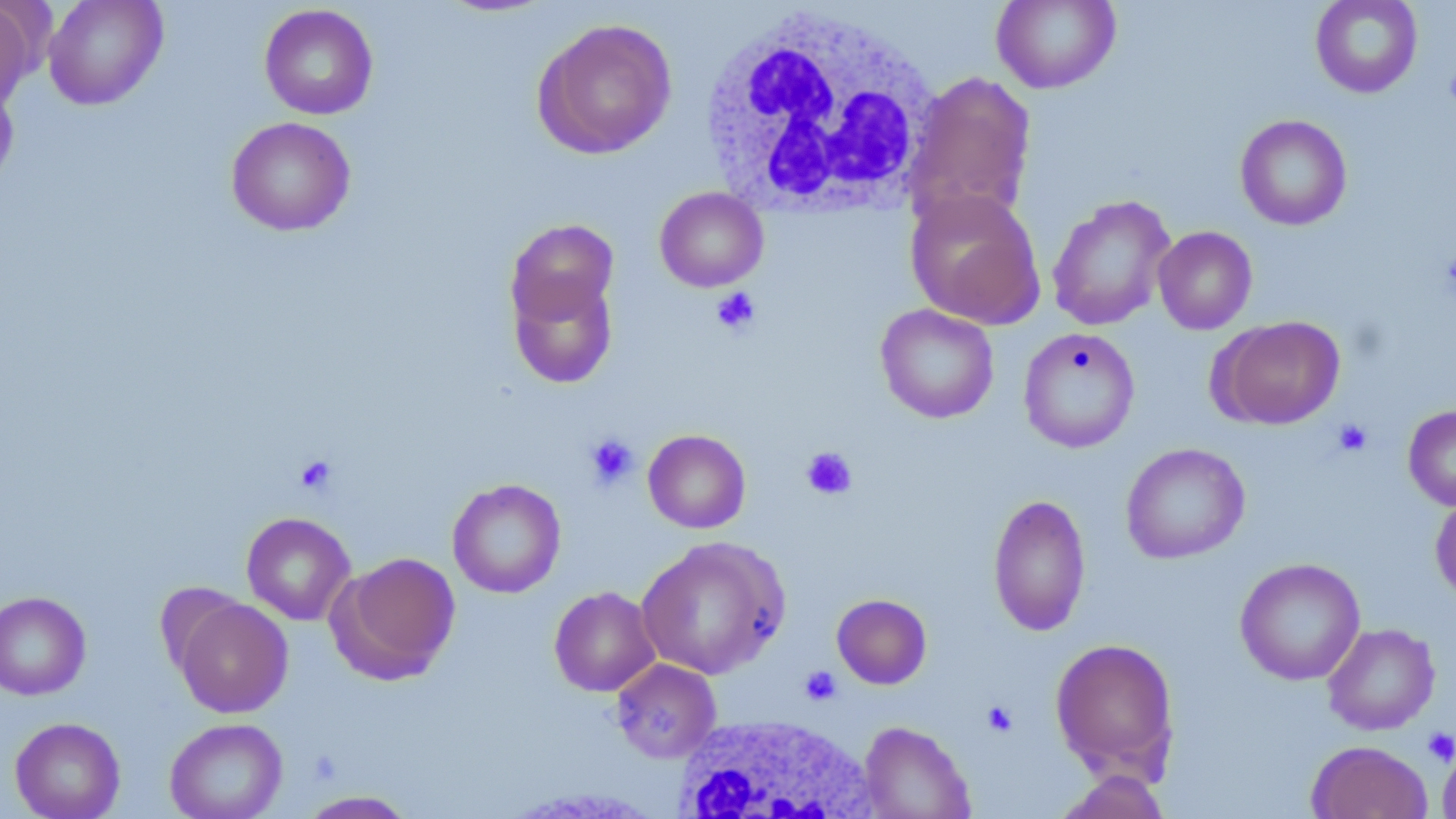

{
  "slide_level_diagnosis": "no evidence of blood parasites",
  "modality": "optical microscopy",
  "preparation": "thin blood smear",
  "uninfected_red_blood_cell_locations": "approximate bounding boxes as named x1/y1/x2/y2 corners in pixels: (x1=42, y1=0, x2=168, y2=110), (x1=991, y1=0, x2=1120, y2=93), (x1=1310, y1=0, x2=1423, y2=98), (x1=0, y1=1, x2=37, y2=114), (x1=259, y1=4, x2=379, y2=120), (x1=533, y1=17, x2=677, y2=160), (x1=904, y1=71, x2=1038, y2=229), (x1=0, y1=76, x2=20, y2=193), (x1=1235, y1=114, x2=1352, y2=231), (x1=225, y1=116, x2=356, y2=236), (x1=655, y1=186, x2=768, y2=292), (x1=906, y1=188, x2=1046, y2=330), (x1=1047, y1=194, x2=1176, y2=331), (x1=505, y1=219, x2=620, y2=330), (x1=1153, y1=226, x2=1257, y2=334), (x1=506, y1=265, x2=619, y2=389), (x1=875, y1=304, x2=999, y2=424), (x1=1214, y1=315, x2=1345, y2=429), (x1=1018, y1=327, x2=1140, y2=453), (x1=1403, y1=405, x2=1456, y2=511), (x1=643, y1=429, x2=751, y2=533), (x1=1120, y1=442, x2=1250, y2=564), (x1=447, y1=479, x2=566, y2=599), (x1=1430, y1=492, x2=1456, y2=605), (x1=987, y1=493, x2=1092, y2=637), (x1=241, y1=512, x2=356, y2=625), (x1=635, y1=537, x2=789, y2=680), (x1=331, y1=551, x2=461, y2=683), (x1=1235, y1=557, x2=1365, y2=685), (x1=549, y1=586, x2=661, y2=697), (x1=0, y1=591, x2=91, y2=701), (x1=832, y1=593, x2=932, y2=689), (x1=173, y1=597, x2=293, y2=718), (x1=1322, y1=622, x2=1440, y2=735), (x1=1049, y1=638, x2=1181, y2=784), (x1=611, y1=658, x2=722, y2=763), (x1=10, y1=717, x2=126, y2=819), (x1=164, y1=717, x2=288, y2=819), (x1=859, y1=721, x2=975, y2=819), (x1=1306, y1=740, x2=1433, y2=819), (x1=1436, y1=740, x2=1456, y2=818), (x1=1052, y1=769, x2=1173, y2=819), (x1=296, y1=790, x2=419, y2=818)",
  "magnification": "1000x",
  "stain": "May-Grünwald-Giemsa",
  "field_of_view": "one of a larger specimen",
  "platelet_locations": "approximate bounding boxes as named x1/y1/x2/y2 corners in pixels: (x1=1444, y1=64, x2=1456, y2=110), (x1=711, y1=286, x2=761, y2=336), (x1=1332, y1=418, x2=1373, y2=457), (x1=584, y1=433, x2=639, y2=490), (x1=801, y1=446, x2=857, y2=500), (x1=294, y1=456, x2=338, y2=496), (x1=799, y1=666, x2=841, y2=705), (x1=982, y1=701, x2=1017, y2=737), (x1=1423, y1=727, x2=1456, y2=765)",
  "image_size": "1456×819 pixels",
  "white_blood_cell_locations": "approximate bounding boxes as named x1/y1/x2/y2 corners in pixels: (x1=698, y1=6, x2=940, y2=219), (x1=673, y1=713, x2=878, y2=819)"
}